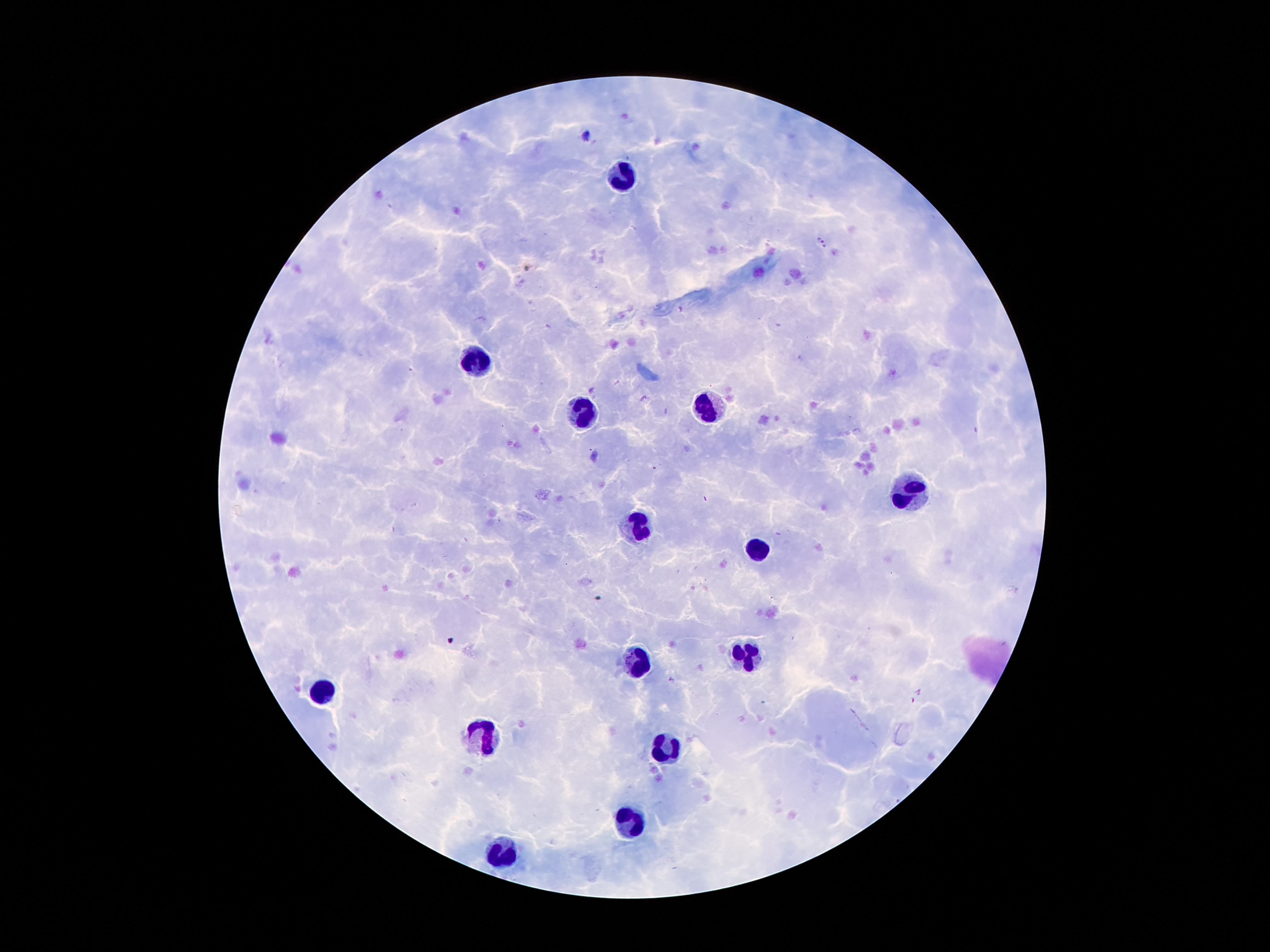 Approximate centers as [x, y] in pixels. Leukocyte locations: [617, 175], [472, 362], [709, 410], [581, 414], [907, 494], [634, 528], [754, 549], [749, 654], [638, 660], [319, 694], [485, 734], [663, 748], [628, 820], [502, 856]. Malaria parasite locations: [820, 238], [824, 248]. Patient malaria status: positive for Plasmodium falciparum. Smartphone photograph taken through the microscope eyepiece. Image is 1270×952 pixels. Thick blood smear. Single field of view. Giemsa stain. 100x magnification.